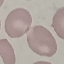

malaria_status: uninfected
stain: Giemsa
capture: smartphone camera at the microscope eyepiece
image_type: automatically extracted cell patch, resized to 64 × 64 pixels
preparation: thin blood film